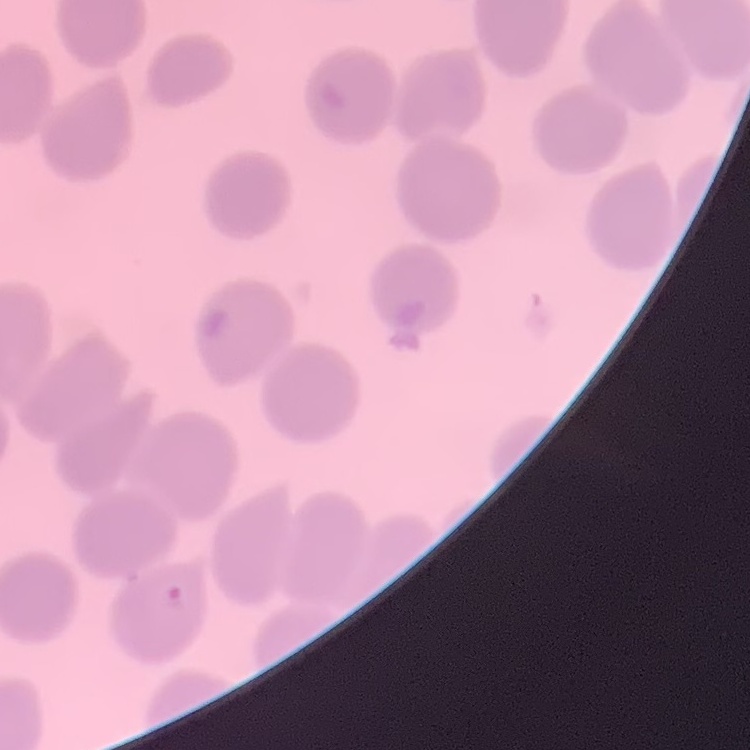

Summary:
  - Red blood cell morphology: no rouleaux formation
  - Preparation: thin peripheral smear
  - Image type: square crop of a larger photomicrograph
  - Stain: Field's or Giemsa